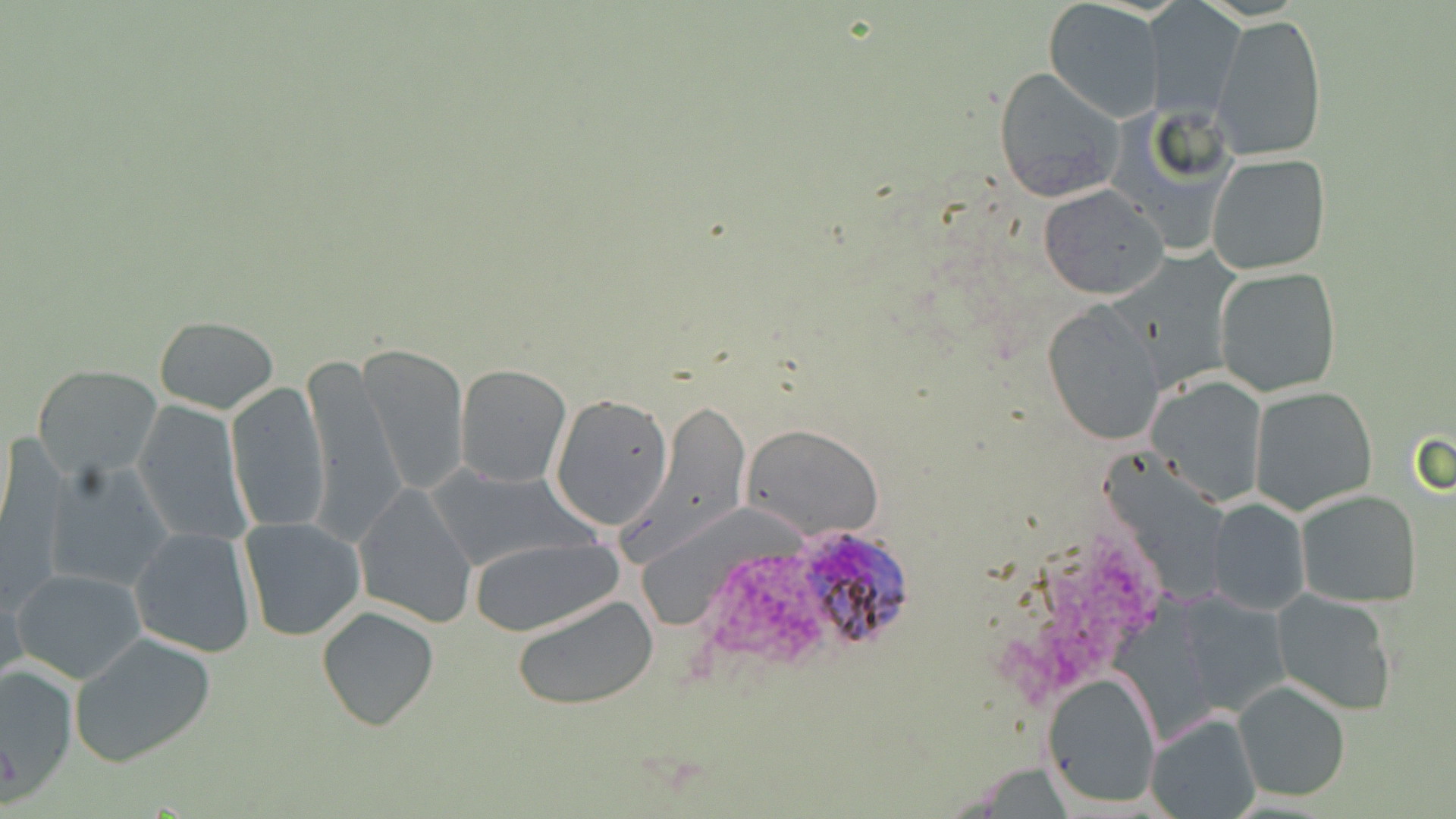
{
  "slide_level_diagnosis": "Plasmodium ovale",
  "image_size": "1456×819 pixels",
  "preparation": "thin blood smear",
  "field_of_view": "one of a larger specimen",
  "plasmodium_ovale_infected_red_blood_cell_locations": "approximate bounding boxes as (x1,y1)-(x2,y2) corner pairs in pixels: (785,525)-(906,657)",
  "modality": "optical microscopy",
  "magnification": "1000x",
  "uninfected_red_blood_cell_locations": "approximate bounding boxes as (x1,y1)-(x2,y2) corner pairs in pixels: (1042,0)-(1163,121), (1146,2)-(1244,117), (1211,13)-(1327,163), (993,67)-(1124,203), (1206,154)-(1330,275), (1038,184)-(1167,300), (1214,266)-(1343,398), (1042,302)-(1166,446), (153,316)-(278,415), (356,343)-(471,494), (303,358)-(403,542), (455,363)-(573,487), (34,364)-(159,479), (1147,374)-(1269,504), (226,379)-(330,534), (1249,385)-(1379,516), (550,394)-(674,528), (134,399)-(250,543), (638,401)-(750,555), (741,423)-(884,539), (42,459)-(175,593), (427,464)-(598,572), (355,484)-(477,627), (1294,489)-(1422,607), (1209,496)-(1310,614), (238,517)-(367,641), (128,525)-(258,659), (468,535)-(624,636), (11,567)-(148,684), (0,582)-(26,698), (1272,588)-(1399,716), (1172,592)-(1292,719), (515,594)-(660,710), (315,605)-(440,732), (68,632)-(218,769), (0,663)-(78,796), (1041,669)-(1162,810), (1233,680)-(1354,801), (1143,711)-(1260,819)",
  "stain": "May-Grünwald-Giemsa"
}